Outline each blood parasite and name the species.
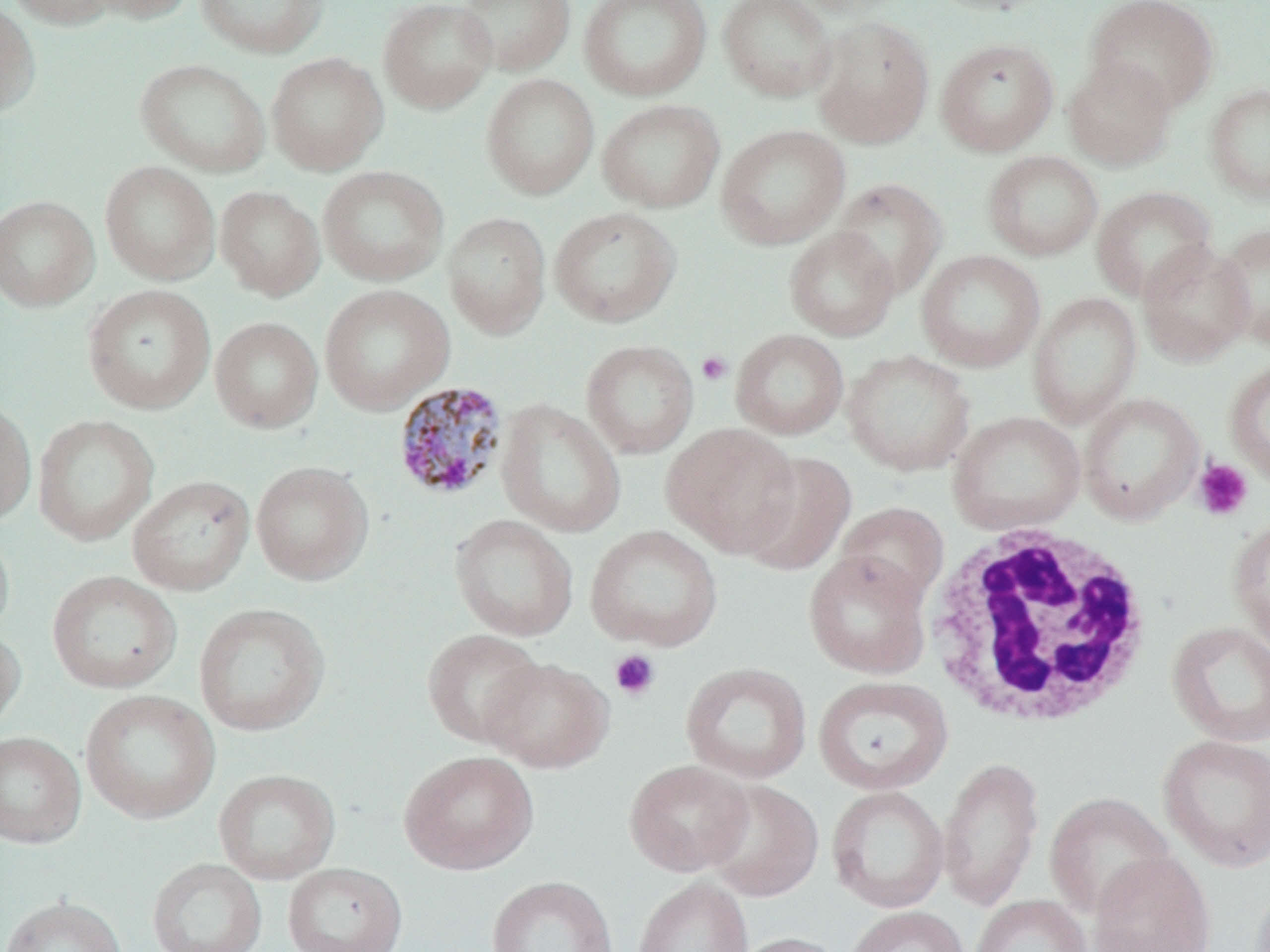
Approximate bounding boxes as (x1, y1, x2, y2) in pixels.
Plasmodium malariae-infected red blood cells: (393, 380, 509, 501).
No Plasmodium falciparum, Plasmodium ovale, Plasmodium vivax, Babesia divergens, or Trypanosoma brucei observed.

White blood cell locations: (922, 523, 1153, 730). Uninfected red blood cell locations (subset): (3, 0, 118, 29), (81, 0, 197, 23), (195, 0, 330, 59), (378, 0, 497, 114), (456, 0, 575, 77), (578, 0, 713, 102), (717, 0, 838, 103), (788, 0, 913, 18), (924, 0, 1058, 16), (1084, 0, 1219, 112), (0, 2, 41, 118), (811, 16, 935, 149), (935, 37, 1059, 157), (266, 51, 388, 176), (1062, 56, 1177, 171), (135, 58, 271, 177), (481, 73, 599, 200), (1204, 82, 1270, 204), (597, 99, 725, 213), (715, 124, 850, 250), (982, 150, 1103, 261), (100, 161, 220, 285), (318, 165, 449, 286), (832, 178, 947, 299), (1091, 185, 1215, 302), (215, 186, 324, 300), (0, 195, 99, 312), (548, 206, 681, 328), (442, 210, 551, 340), (1215, 222, 1270, 352), (784, 226, 900, 342), (1136, 241, 1254, 366), (916, 249, 1045, 372), (83, 284, 215, 414), (318, 284, 455, 415), (1027, 292, 1142, 429), (210, 317, 323, 433), (731, 329, 849, 440), (581, 339, 699, 459), (842, 349, 975, 476), (1224, 360, 1270, 487), (0, 396, 37, 526), (495, 399, 626, 538), (947, 410, 1086, 534), (32, 414, 159, 546), (662, 423, 802, 557), (737, 450, 857, 577), (251, 461, 373, 585), (127, 475, 255, 596), (834, 501, 949, 608), (449, 513, 579, 641), (1227, 517, 1270, 651), (0, 523, 15, 643), (584, 525, 723, 652), (802, 550, 932, 679), (46, 570, 182, 693), (193, 602, 330, 736), (1165, 620, 1270, 747), (0, 624, 26, 735), (422, 628, 544, 747), (481, 656, 614, 773), (680, 661, 812, 784), (812, 675, 953, 795), (79, 688, 220, 824), (0, 731, 86, 848), (1156, 733, 1270, 872), (398, 750, 539, 875), (937, 756, 1044, 911), (624, 759, 754, 876), (214, 768, 340, 885), (703, 780, 824, 902), (827, 785, 949, 913), (1044, 791, 1175, 918), (1088, 851, 1216, 952), (147, 857, 267, 952), (283, 862, 408, 952), (486, 875, 617, 952), (633, 876, 753, 952), (969, 894, 1091, 952), (0, 895, 128, 952), (844, 905, 969, 952), (730, 932, 848, 952). Platelet locations (subset): (696, 351, 732, 386), (1192, 458, 1254, 521), (609, 649, 661, 701). Slide-level diagnosis: Plasmodium malariae. One field of a larger specimen. Thin blood film. Captured at 1000x magnification. May-Grünwald-Giemsa-stained preparation. Image is 1270×952 pixels. Light microscopy.